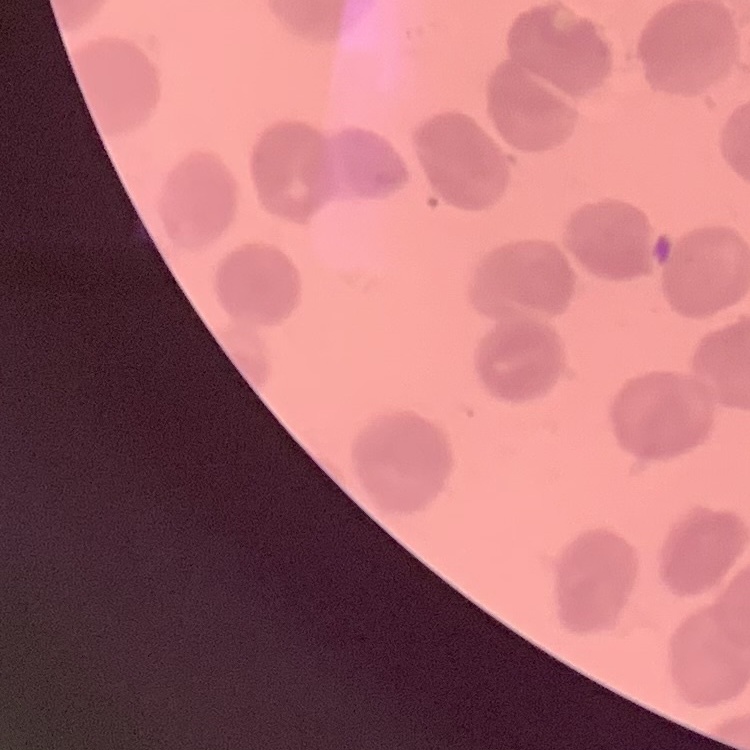

red blood cell morphology = no rouleaux formation
image type = one tile cut from a larger photomicrograph
preparation = thin blood film
stain = Field's or Giemsa